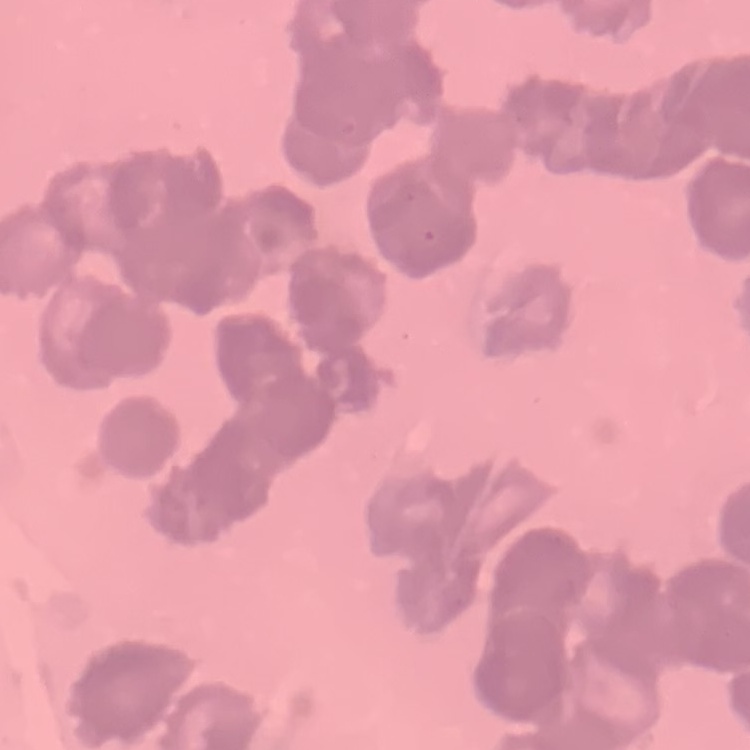

Summary:
  - Red blood cell morphology: rouleaux formation
  - Stain: Field's or Giemsa
  - Preparation: thin peripheral smear
  - Image type: one tile cut from a larger photomicrograph